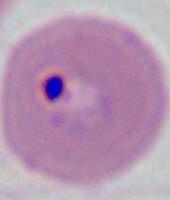

identification = Plasmodium
magnification = 400x or 1000x
modality = micrograph